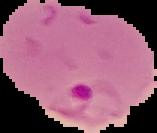

Summary:
  - Image type: cell region segmented out of the field of view; surrounding area masked to black
  - Preparation: thin blood film
  - Image size: 157×133 pixels
  - Malaria status: parasitized